Assess this cell for malaria.
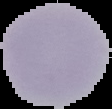

Uninfected.

image type = segmented cell region with the area outside set to black
image size = 112×109 pixels
preparation = thin blood smear